Comment on the morphology of the erythrocytes.
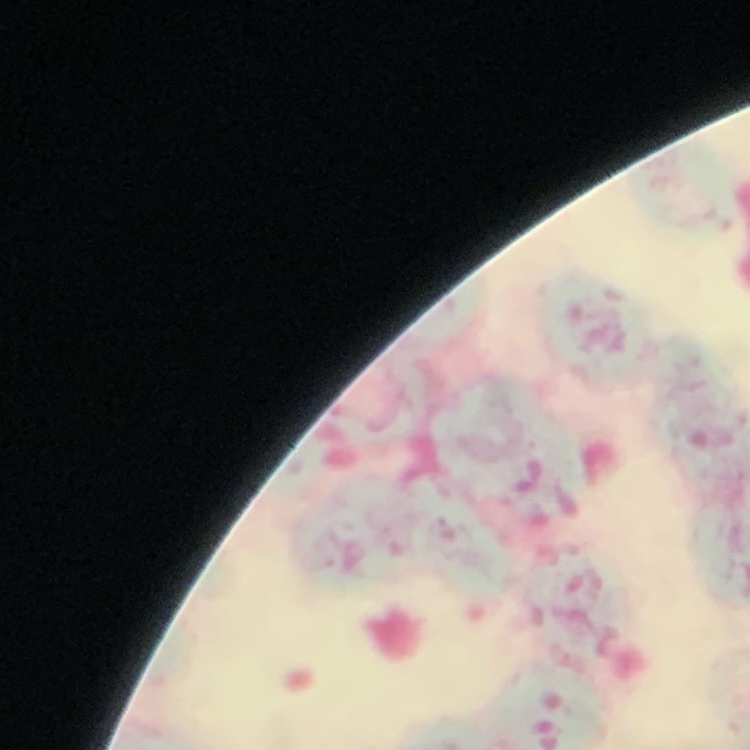

They show rouleaux formation.

{
  "preparation": "thin peripheral smear",
  "stain": "Field's or Giemsa",
  "image_type": "square crop of a larger photomicrograph"
}